Give the position of every malaria parasite.
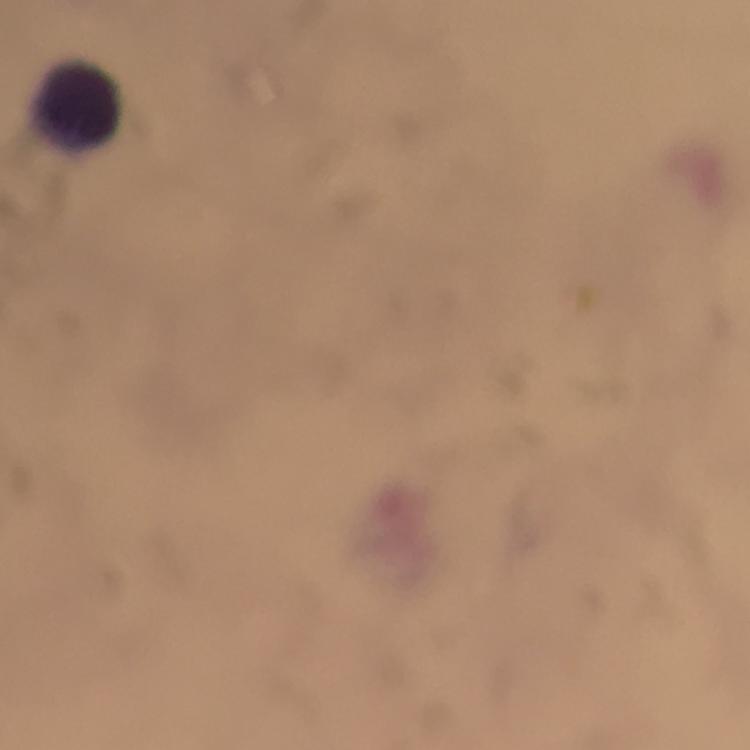

No malaria parasites detected.

Approximate object centers, in pixels from the top-left corner. Leukocyte locations: (x=81, y=101). Smartphone photograph taken through a microscope. Cropped region of a single field of view. Immersion oil was used. At 100x magnification. Giemsa stain. Image is 750×750 pixels. Thick blood film. From a diagnostic examination for malaria.